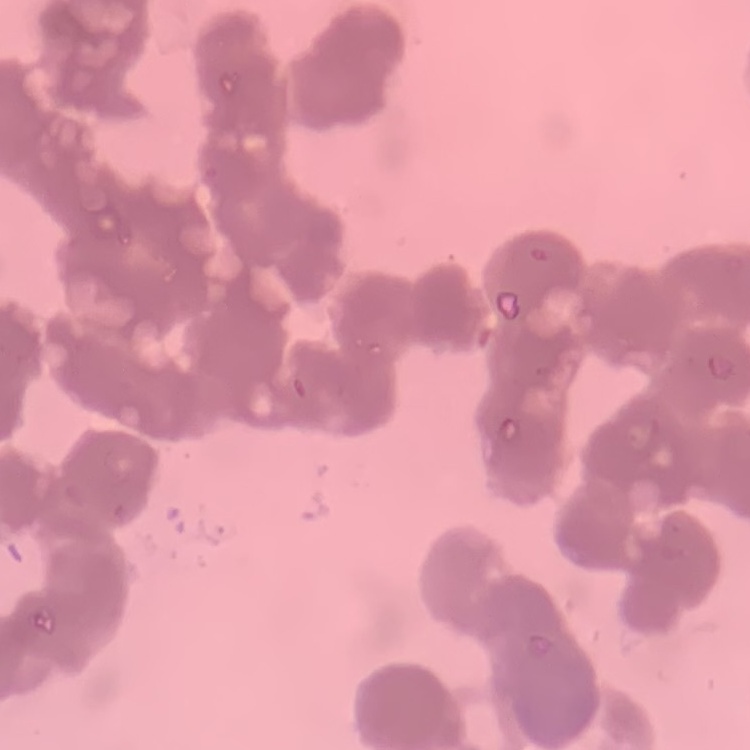 The erythrocytes exhibit rouleaux formation. Square crop of a larger photomicrograph. Stained with either Field's or Giemsa. Thin blood smear.